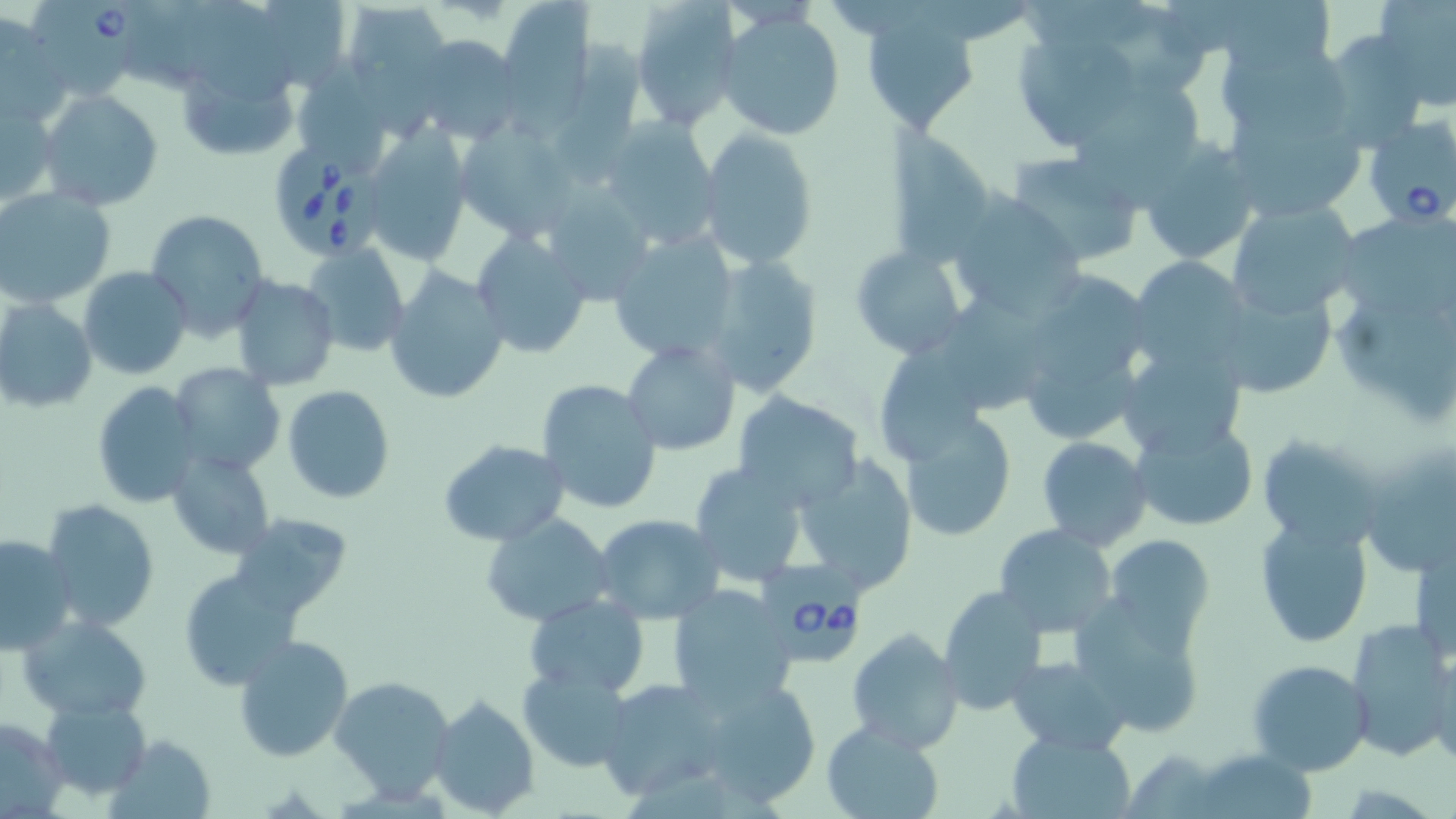 Approximate bounding boxes as named x1/y1/x2/y2 corners in pixels. Babesia divergens-infected red blood cell locations: (x1=31, y1=1, x2=149, y2=97), (x1=1361, y1=112, x2=1456, y2=230), (x1=273, y1=139, x2=381, y2=259), (x1=764, y1=557, x2=865, y2=670). Uninfected red blood cell locations: (x1=266, y1=0, x2=350, y2=92), (x1=500, y1=0, x2=590, y2=107), (x1=628, y1=0, x2=740, y2=130), (x1=1222, y1=0, x2=1335, y2=69), (x1=1375, y1=0, x2=1456, y2=105), (x1=341, y1=1, x2=451, y2=86), (x1=178, y1=2, x2=301, y2=104), (x1=863, y1=4, x2=981, y2=136), (x1=1084, y1=5, x2=1208, y2=93), (x1=717, y1=8, x2=847, y2=141), (x1=2, y1=11, x2=62, y2=123), (x1=1318, y1=33, x2=1430, y2=146), (x1=409, y1=34, x2=521, y2=142), (x1=558, y1=35, x2=647, y2=190), (x1=1019, y1=35, x2=1137, y2=144), (x1=1221, y1=48, x2=1348, y2=145), (x1=177, y1=60, x2=303, y2=161), (x1=299, y1=67, x2=385, y2=173), (x1=1069, y1=81, x2=1204, y2=201), (x1=37, y1=90, x2=163, y2=211), (x1=1223, y1=93, x2=1371, y2=222), (x1=2, y1=100, x2=57, y2=208), (x1=600, y1=118, x2=723, y2=252), (x1=458, y1=125, x2=577, y2=243), (x1=696, y1=130, x2=818, y2=269), (x1=360, y1=131, x2=470, y2=264), (x1=1134, y1=135, x2=1263, y2=266), (x1=885, y1=136, x2=994, y2=265), (x1=1005, y1=152, x2=1144, y2=266), (x1=551, y1=182, x2=648, y2=305), (x1=0, y1=185, x2=116, y2=308), (x1=945, y1=197, x2=1085, y2=320), (x1=1227, y1=199, x2=1363, y2=319), (x1=144, y1=208, x2=270, y2=340), (x1=1346, y1=215, x2=1456, y2=323), (x1=469, y1=230, x2=593, y2=358), (x1=607, y1=231, x2=741, y2=366), (x1=303, y1=243, x2=411, y2=359), (x1=849, y1=245, x2=970, y2=360), (x1=701, y1=253, x2=823, y2=397), (x1=1129, y1=257, x2=1253, y2=376), (x1=384, y1=265, x2=509, y2=405), (x1=79, y1=267, x2=193, y2=380), (x1=1040, y1=274, x2=1158, y2=380), (x1=230, y1=275, x2=339, y2=390), (x1=1213, y1=283, x2=1336, y2=400), (x1=947, y1=297, x2=1055, y2=406), (x1=0, y1=298, x2=97, y2=413), (x1=1342, y1=298, x2=1456, y2=416), (x1=866, y1=336, x2=993, y2=463), (x1=623, y1=338, x2=741, y2=455), (x1=1028, y1=362, x2=1139, y2=438), (x1=169, y1=363, x2=284, y2=478), (x1=1135, y1=366, x2=1252, y2=457), (x1=536, y1=378, x2=663, y2=515), (x1=89, y1=382, x2=201, y2=507), (x1=283, y1=385, x2=395, y2=502), (x1=732, y1=392, x2=865, y2=512), (x1=900, y1=413, x2=1017, y2=541), (x1=1128, y1=416, x2=1258, y2=532), (x1=1256, y1=433, x2=1385, y2=553), (x1=1037, y1=437, x2=1153, y2=551), (x1=438, y1=438, x2=569, y2=545), (x1=1356, y1=444, x2=1456, y2=580), (x1=168, y1=449, x2=274, y2=559), (x1=790, y1=456, x2=919, y2=596), (x1=689, y1=462, x2=813, y2=587), (x1=41, y1=499, x2=160, y2=632), (x1=228, y1=512, x2=353, y2=617), (x1=481, y1=512, x2=614, y2=627), (x1=591, y1=512, x2=725, y2=624), (x1=1253, y1=517, x2=1373, y2=648), (x1=994, y1=525, x2=1118, y2=637), (x1=0, y1=533, x2=78, y2=655), (x1=1104, y1=534, x2=1215, y2=646), (x1=177, y1=566, x2=306, y2=689), (x1=668, y1=583, x2=801, y2=707), (x1=937, y1=583, x2=1048, y2=715), (x1=524, y1=594, x2=650, y2=697), (x1=1071, y1=596, x2=1208, y2=738), (x1=19, y1=612, x2=152, y2=720), (x1=1344, y1=618, x2=1456, y2=764), (x1=846, y1=629, x2=964, y2=753), (x1=232, y1=635, x2=354, y2=762), (x1=1432, y1=652, x2=1455, y2=773), (x1=1006, y1=654, x2=1130, y2=753), (x1=1246, y1=657, x2=1373, y2=776), (x1=519, y1=666, x2=633, y2=770), (x1=691, y1=673, x2=823, y2=808), (x1=330, y1=674, x2=456, y2=800), (x1=596, y1=678, x2=731, y2=802), (x1=428, y1=695, x2=538, y2=818), (x1=42, y1=698, x2=151, y2=800), (x1=0, y1=715, x2=67, y2=815), (x1=820, y1=721, x2=946, y2=819), (x1=1007, y1=730, x2=1135, y2=817), (x1=108, y1=734, x2=216, y2=819), (x1=1123, y1=747, x2=1231, y2=817), (x1=1197, y1=748, x2=1315, y2=819). Slide-level diagnosis: Babesia divergens. 1000x magnification. Thin blood smear. May-Grünwald-Giemsa stain. One field of a larger specimen. Image is 1456×819 pixels. Optical microscopy.